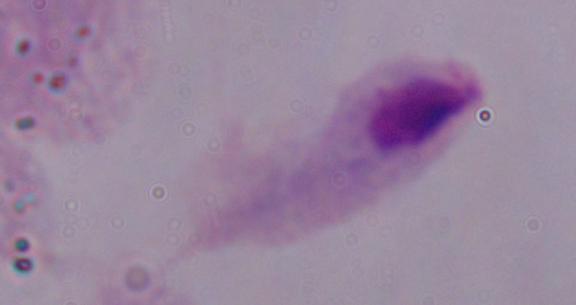
identification: trichomonad
modality: micrograph
magnification: 1000x